Give the position of every Plasmodium parasite visible.
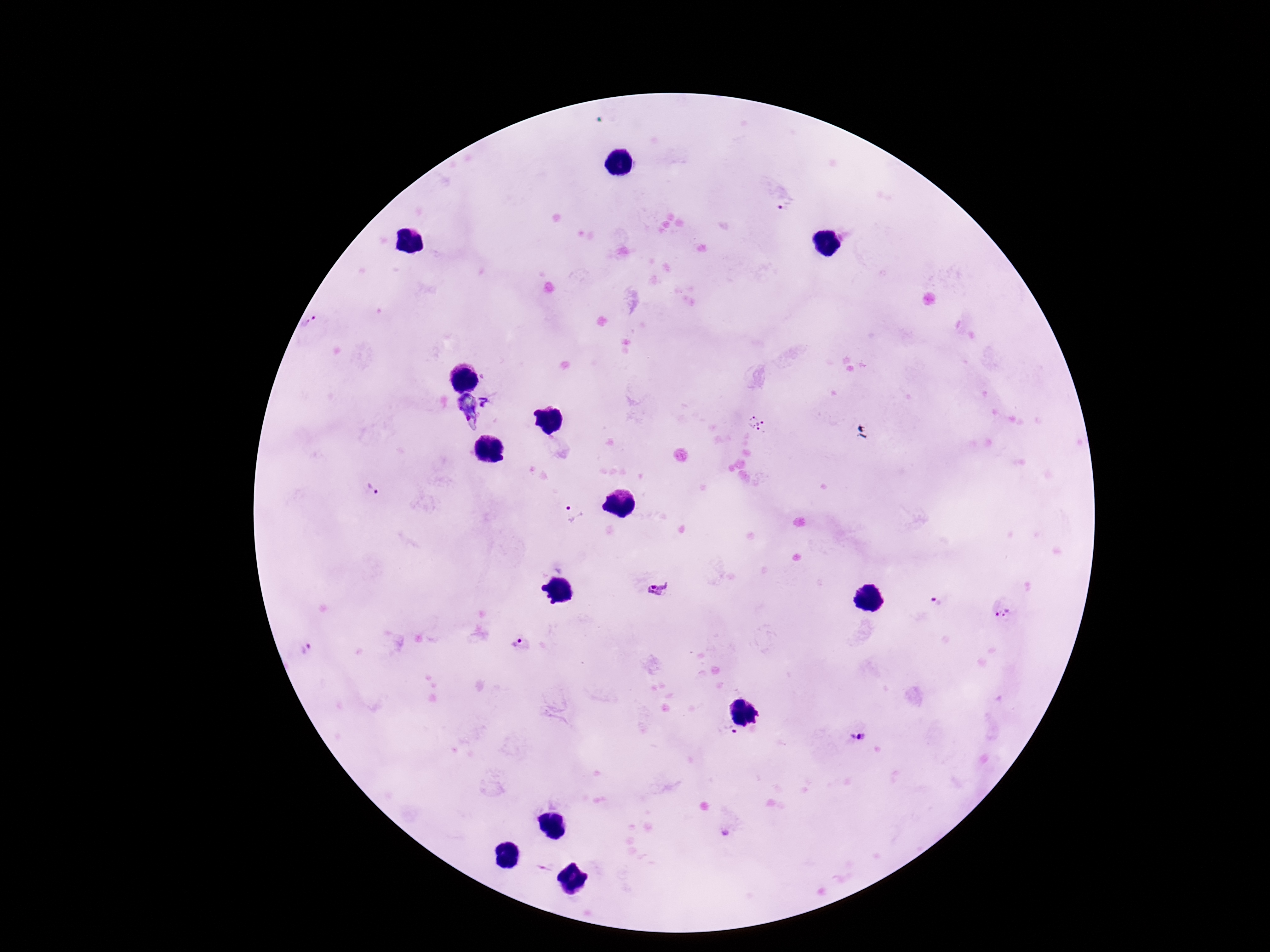

Approximate centers as {x, y} in pixels.
Plasmodium parasites: {786, 204}, {312, 325}, {470, 408}, {756, 423}, {372, 491}, {572, 513}, {659, 589}, {939, 601}, {1002, 611}, {518, 642}, {309, 649}, {855, 737}.

Summary:
  - Stain: Giemsa
  - Preparation: thick peripheral-blood smear
  - Image size: 1270×952 pixels
  - Capture: smartphone camera through the microscope eyepiece
  - Patient malaria status: positive
  - Field of view: one from this slide
  - Magnification: 100x